Point out each leukocyte.
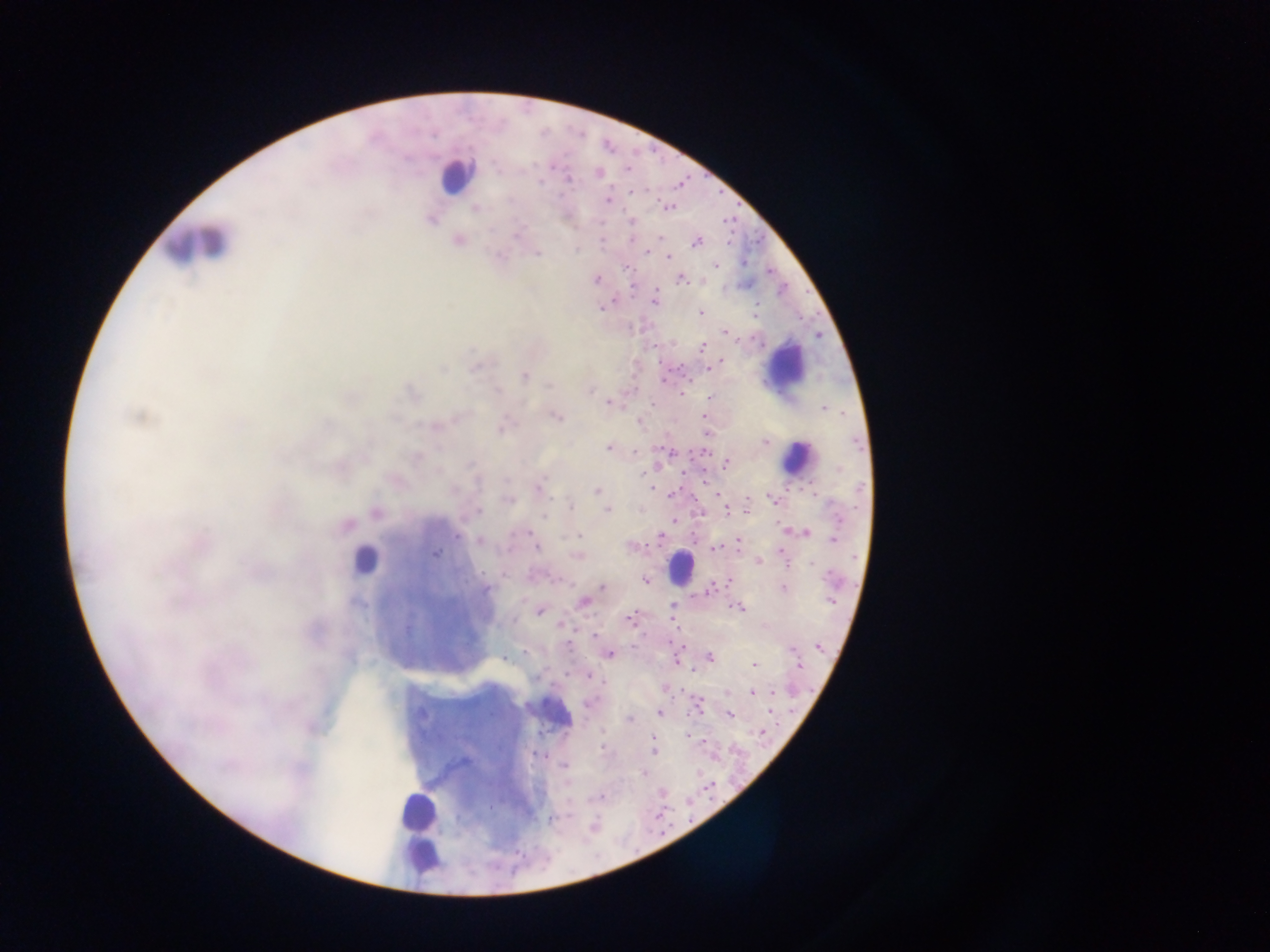

Approximate centers as (x, y) in pixels.
Leukocytes: (456, 174), (193, 242), (784, 364), (798, 458), (363, 560), (681, 566), (551, 711), (418, 810), (422, 829), (419, 854).

Summary:
  - Plasmodium parasite locations: (627, 169), (599, 173), (569, 179), (540, 182), (633, 192), (608, 200), (510, 201), (475, 207), (669, 208), (631, 221), (516, 236), (660, 237), (602, 241), (697, 243), (648, 252), (537, 253), (668, 256), (717, 265), (681, 279), (597, 280), (654, 301), (601, 308), (701, 313), (725, 332), (702, 348), (721, 362), (713, 366), (476, 367), (710, 368), (442, 369), (524, 375), (549, 386), (498, 390), (589, 391), (681, 393), (710, 398), (608, 402), (824, 409), (138, 417), (556, 417), (704, 417), (639, 421), (502, 428), (765, 443), (609, 447), (703, 451), (635, 452), (670, 453), (726, 463), (839, 469), (642, 473), (539, 486), (596, 491), (673, 493), (508, 500), (773, 500), (570, 506), (746, 508), (607, 509), (479, 510), (727, 511), (376, 512), (544, 517), (838, 519), (674, 521), (346, 525), (784, 530), (527, 532), (807, 532), (457, 536), (579, 536), (660, 537), (479, 539), (834, 539), (737, 541), (534, 543), (537, 547), (630, 547), (715, 548), (435, 554), (576, 556), (759, 561), (812, 564), (483, 573), (831, 579), (645, 580), (729, 580), (711, 587), (782, 587), (603, 588), (486, 589), (592, 594), (830, 601), (583, 602), (672, 607), (738, 608), (539, 611), (629, 618), (513, 621), (560, 625), (407, 630), (594, 635), (568, 645), (819, 646), (791, 649), (524, 652), (609, 654), (510, 656), (710, 657), (504, 658), (754, 665), (799, 665), (592, 678), (536, 679), (604, 683), (774, 691), (752, 692), (727, 693), (771, 695), (588, 704), (659, 713), (729, 715), (629, 720), (761, 733), (687, 734), (652, 739), (602, 747), (653, 751), (564, 765), (643, 773), (602, 797), (490, 807), (551, 818)
  - Image size: 1270×952 pixels
  - Preparation: thick blood smear
  - Field of view: single
  - Capture: mobile-phone photograph through a microscope
  - Country: Ghana